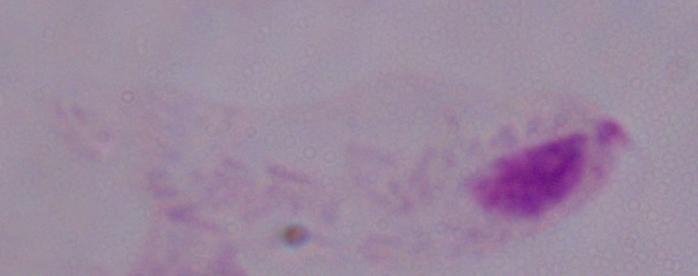

identification = trichomonad
modality = photomicrograph
magnification = 1000x